Assess this cell for malaria.
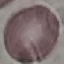
Uninfected.

Summary:
  - Capture: smartphone camera at the microscope eyepiece
  - Preparation: thin smear
  - Image type: automatically extracted cell patch, resized to 64 × 64 pixels
  - Stain: Giemsa